Name the blood parasite species.
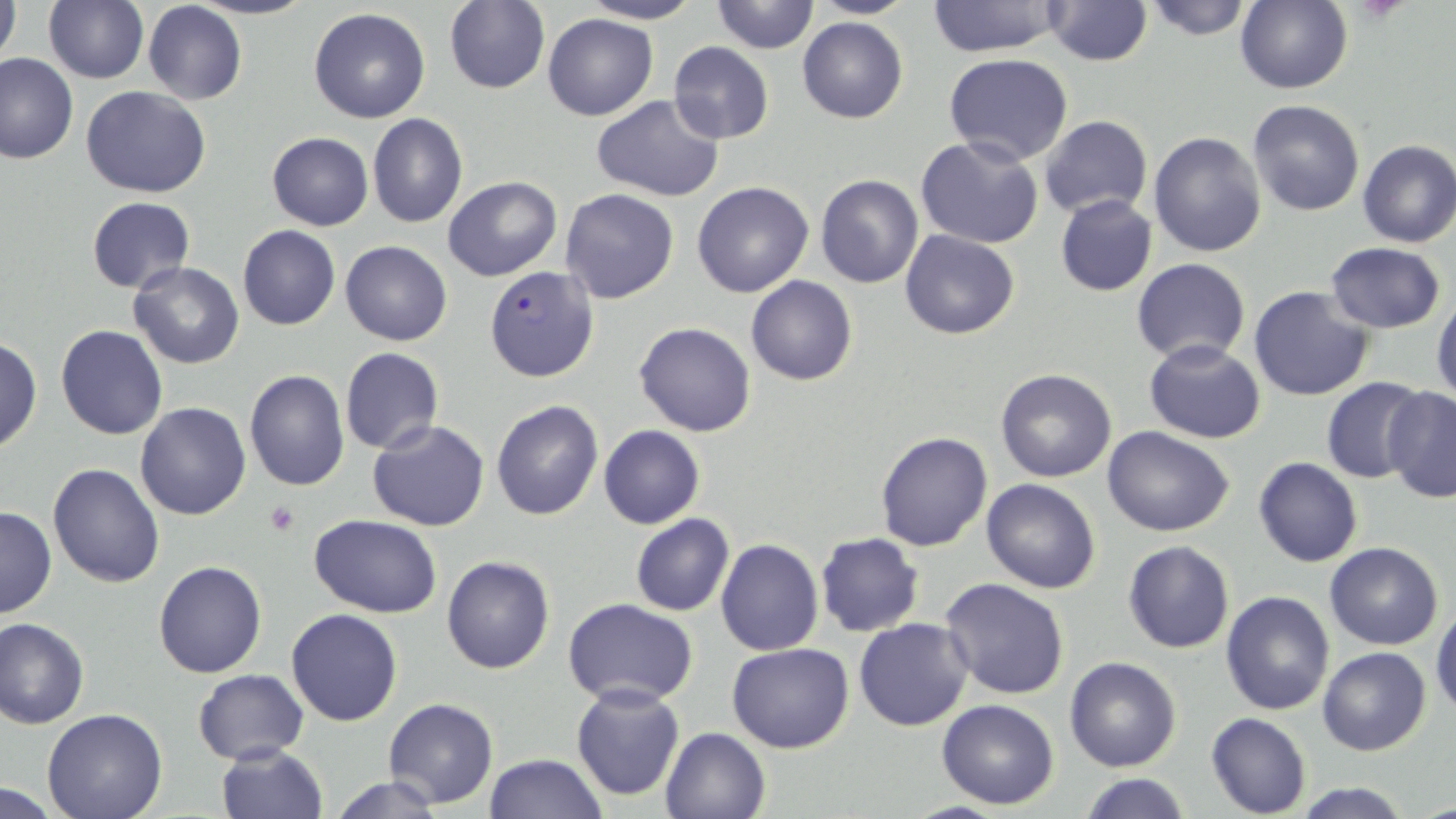

Plasmodium falciparum.

Approximate bounding boxes as (x1,y1)-(x2,y2) corner pairs in pixels. Plasmodium falciparum-infected red blood cell locations: (483,266)-(599,382). Uninfected red blood cell locations: (0,0)-(21,80), (43,0)-(149,85), (189,0)-(316,20), (577,0)-(704,24), (803,0)-(920,20), (927,0)-(1060,58), (1042,0)-(1153,67), (1139,0)-(1257,39), (444,1)-(549,94), (712,1)-(817,53), (1233,1)-(1352,93), (143,2)-(247,105), (309,9)-(430,123), (543,13)-(658,120), (797,16)-(908,123), (667,40)-(774,143), (0,53)-(78,164), (943,54)-(1074,167), (82,86)-(213,198), (591,94)-(725,204), (1247,100)-(1366,218), (1164,106)-(1327,237), (366,112)-(468,229), (1039,115)-(1152,220), (266,132)-(373,230), (1148,132)-(1267,259), (915,136)-(1045,249), (1356,140)-(1456,248), (443,176)-(562,281), (815,176)-(924,289), (692,182)-(814,298), (559,188)-(679,304), (1055,194)-(1158,296), (86,197)-(195,293), (238,225)-(339,330), (900,230)-(1020,340), (340,241)-(452,346), (1325,242)-(1447,333), (1132,257)-(1251,363), (129,261)-(243,368), (746,276)-(857,385), (1248,285)-(1375,401), (1432,297)-(1456,409), (634,320)-(757,437), (57,325)-(168,440), (0,338)-(42,453), (1144,340)-(1265,444), (339,347)-(444,456), (995,367)-(1117,483), (244,371)-(349,491), (1320,375)-(1428,483), (1380,385)-(1455,503), (490,398)-(604,520), (135,402)-(250,519), (366,419)-(490,532), (598,425)-(705,529), (1103,426)-(1235,537), (874,430)-(994,550), (1253,457)-(1362,567), (47,462)-(164,586), (981,478)-(1101,594), (0,507)-(56,619), (630,514)-(734,616), (310,515)-(441,617), (813,532)-(924,638), (715,539)-(823,656), (1122,541)-(1234,653), (1324,541)-(1444,649), (441,556)-(555,674), (153,560)-(267,678), (941,578)-(1071,700), (1221,590)-(1335,716), (563,597)-(699,708), (852,600)-(1067,719), (1431,604)-(1456,718), (286,608)-(403,726), (0,617)-(90,728), (854,618)-(973,732), (727,642)-(853,752), (1318,646)-(1432,757), (1064,656)-(1182,772), (193,668)-(311,764), (571,684)-(685,803), (384,697)-(498,808), (936,697)-(1059,808), (41,709)-(167,819), (1205,713)-(1312,818), (659,726)-(769,819), (215,742)-(328,819), (483,753)-(607,819), (1078,774)-(1195,818), (324,775)-(451,818), (1287,780)-(1416,818), (0,782)-(72,816). Platelet locations: (265,501)-(299,535). Image is 1456×819 pixels. May-Grünwald-Giemsa-stained preparation. Captured at 1000x magnification. Thin blood smear. Optical microscopy. One field of a larger specimen.